Assess the morphology of the red blood cells.
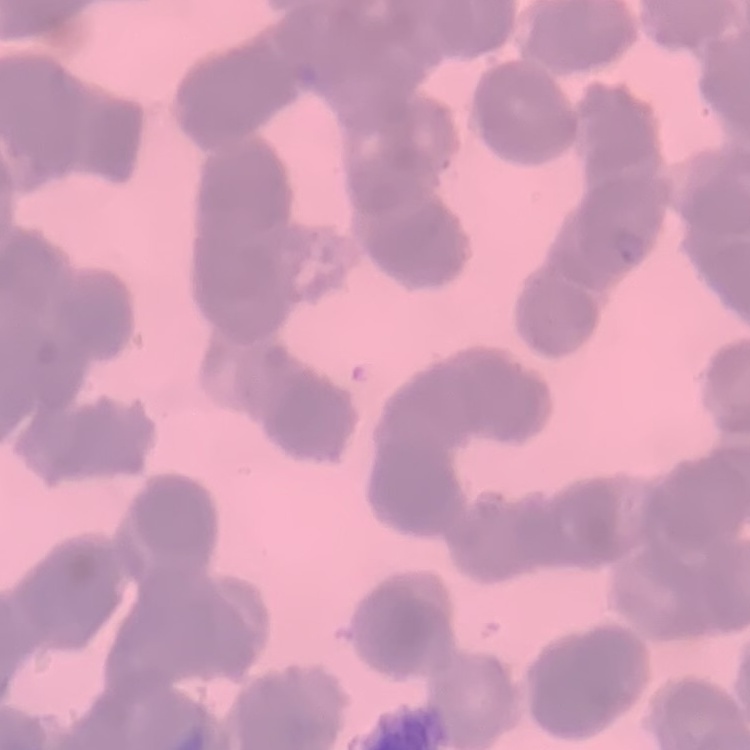
They show rouleaux formation.

One tile cut from a larger photomicrograph. Stained with either Field's or Giemsa. Thin blood smear.